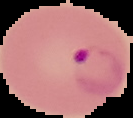
Segmented cell region on a black background. From a thin blood film. Result: malaria parasites detected. Image is 133×118 pixels.